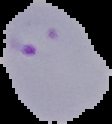
Summary:
  - Image type: segmented cell region on a black background
  - Preparation: thin blood film
  - Image size: 112×124 pixels
  - Result: Plasmodium parasites identified